Describe the morphology of the red blood cells.
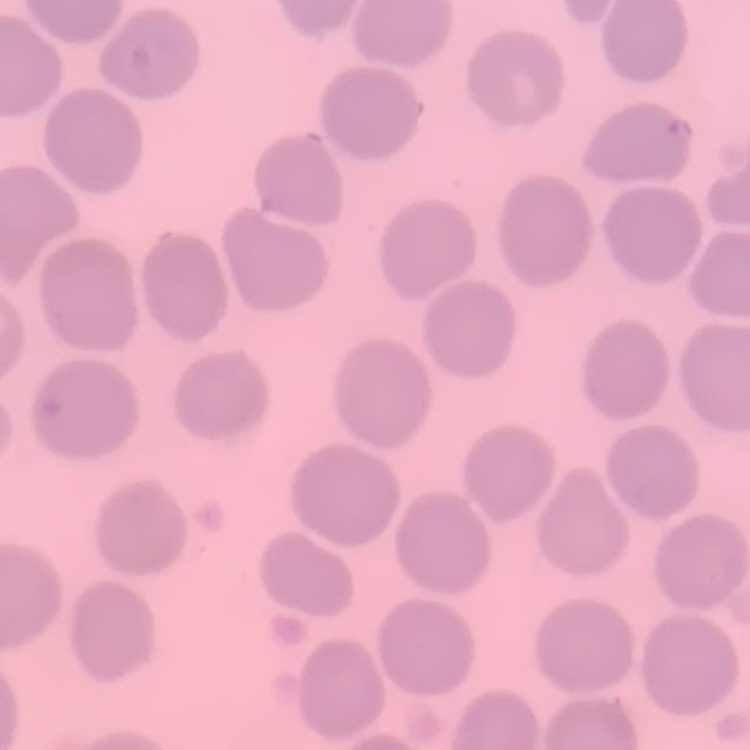

They show no rouleaux formation.

preparation = thin blood film
image type = one tile cut from a larger photomicrograph
stain = Field's or Giemsa